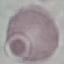 Malaria status: uninfected. Acquired by smartphone through the microscope eyepiece. Giemsa stain. Thin smear of blood. Automatically extracted cell patch, resized to 64 × 64 pixels.